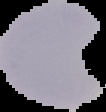

Summary:
  - Result: no malaria parasites detected
  - Preparation: thin blood film
  - Image size: 106×112 pixels
  - Image type: segmented cell region with the area outside set to black